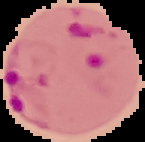
Image is 145×142 pixels. From a thin blood smear. Result: malaria parasites detected. Cell region segmented out of the field of view; the surrounding area is masked to black.